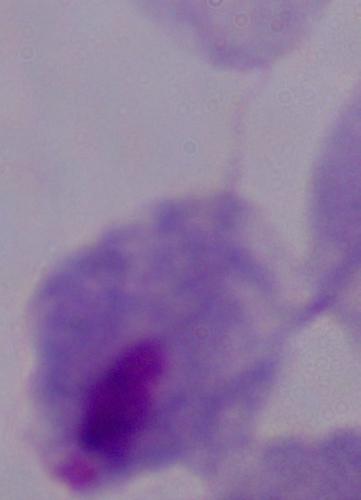 Micrograph. Captured at 1000x magnification. A trichomonad is seen.